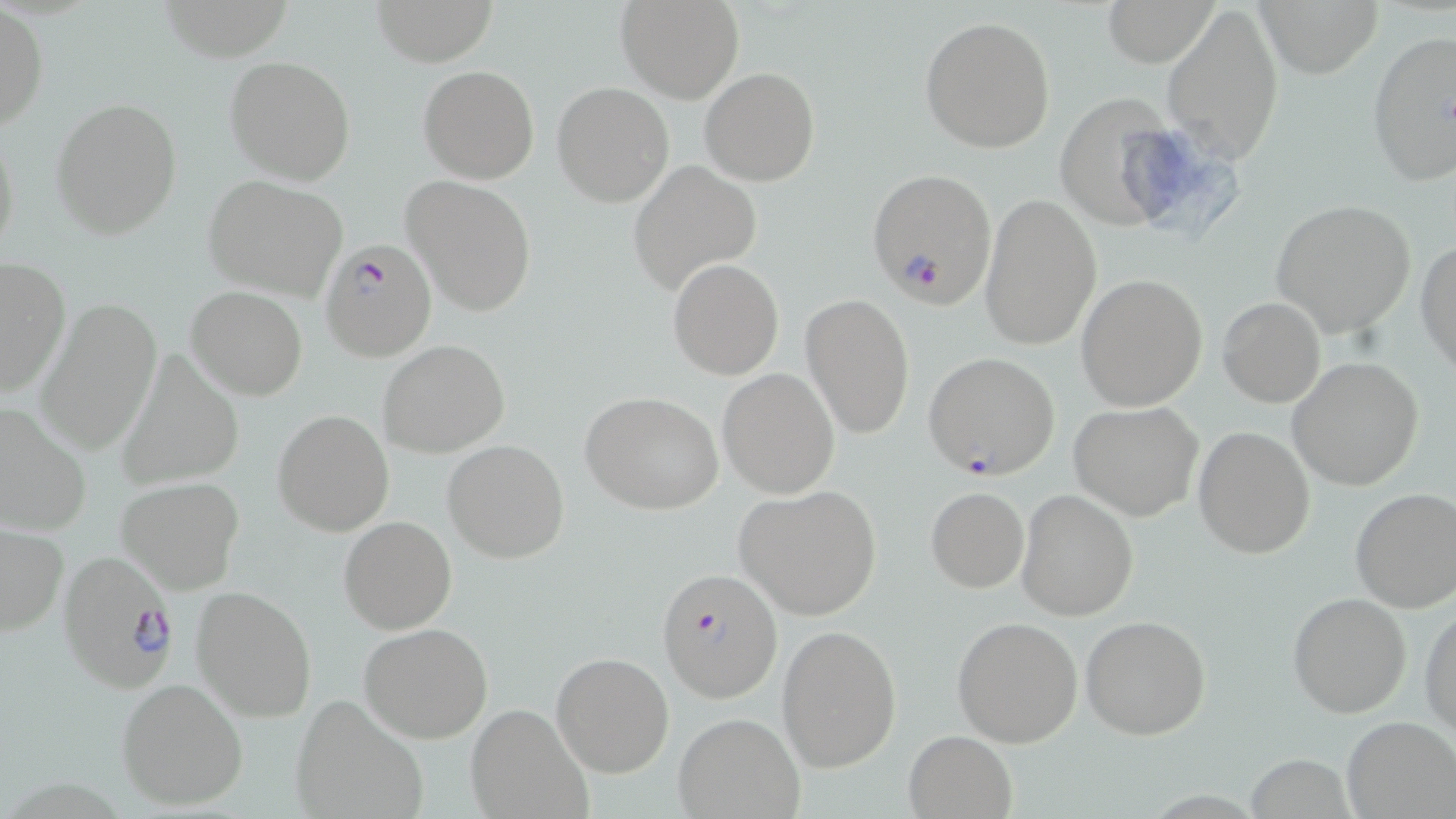

{
  "slide_level_diagnosis": "Plasmodium falciparum",
  "field_of_view": "one of a larger specimen",
  "plasmodium_falciparum_infected_red_blood_cell_locations": "approximate bounding boxes as (x1,y1)-(x2,y2) corner pairs in pixels: (866,167)-(998,309), (319,236)-(438,358), (923,351)-(1061,480), (58,549)-(180,694), (659,569)-(781,700)",
  "modality": "optical microscopy",
  "uninfected_red_blood_cell_locations": "approximate bounding boxes as (x1,y1)-(x2,y2) corner pairs in pixels: (369,0)-(498,66), (615,0)-(744,103), (1104,0)-(1220,67), (1259,0)-(1382,78), (1161,4)-(1285,164), (0,7)-(47,132), (920,16)-(1057,155), (1365,28)-(1455,190), (225,56)-(356,186), (418,65)-(539,184), (700,66)-(820,186), (552,82)-(674,207), (1054,96)-(1181,233), (50,97)-(183,239), (0,122)-(21,268), (630,161)-(760,293), (401,176)-(537,316), (203,177)-(349,300), (980,190)-(1102,352), (1269,199)-(1416,340), (1416,239)-(1456,378), (0,257)-(71,398), (668,259)-(784,380), (1076,273)-(1207,412), (186,287)-(308,400), (801,293)-(916,440), (1218,297)-(1325,408), (35,299)-(162,456), (378,339)-(509,457), (114,352)-(246,490), (1287,356)-(1424,490), (716,367)-(839,499), (582,391)-(725,515), (1069,400)-(1204,520), (0,401)-(92,539), (273,409)-(393,537), (1193,426)-(1315,559), (442,439)-(569,564), (118,477)-(244,594), (734,484)-(883,620), (925,487)-(1028,593), (1016,489)-(1139,621), (1350,489)-(1456,613), (338,515)-(457,634), (1,524)-(68,635), (192,586)-(316,722), (1287,591)-(1412,718), (1421,602)-(1456,738), (1081,615)-(1212,739), (951,617)-(1084,747), (358,622)-(493,743), (777,624)-(902,771), (551,651)-(674,777), (117,677)-(249,811), (290,695)-(428,819), (467,703)-(593,818), (672,711)-(804,819), (1341,715)-(1454,818), (904,730)-(1017,818)",
  "image_size": "1456×819 pixels",
  "magnification": "1000x",
  "preparation": "thin blood smear",
  "stain": "May-Grünwald-Giemsa"
}